Identify the parasite.
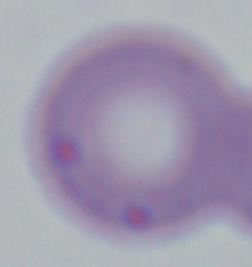
Babesia.

modality = photomicrograph
magnification = 1000x